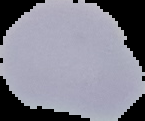
Summary:
  - Image type: segmented cell region on a black background
  - Image size: 145×121 pixels
  - Preparation: thin blood smear
  - Result: negative for malaria parasites